Outline each Plasmodium falciparum-infected red blood cell.
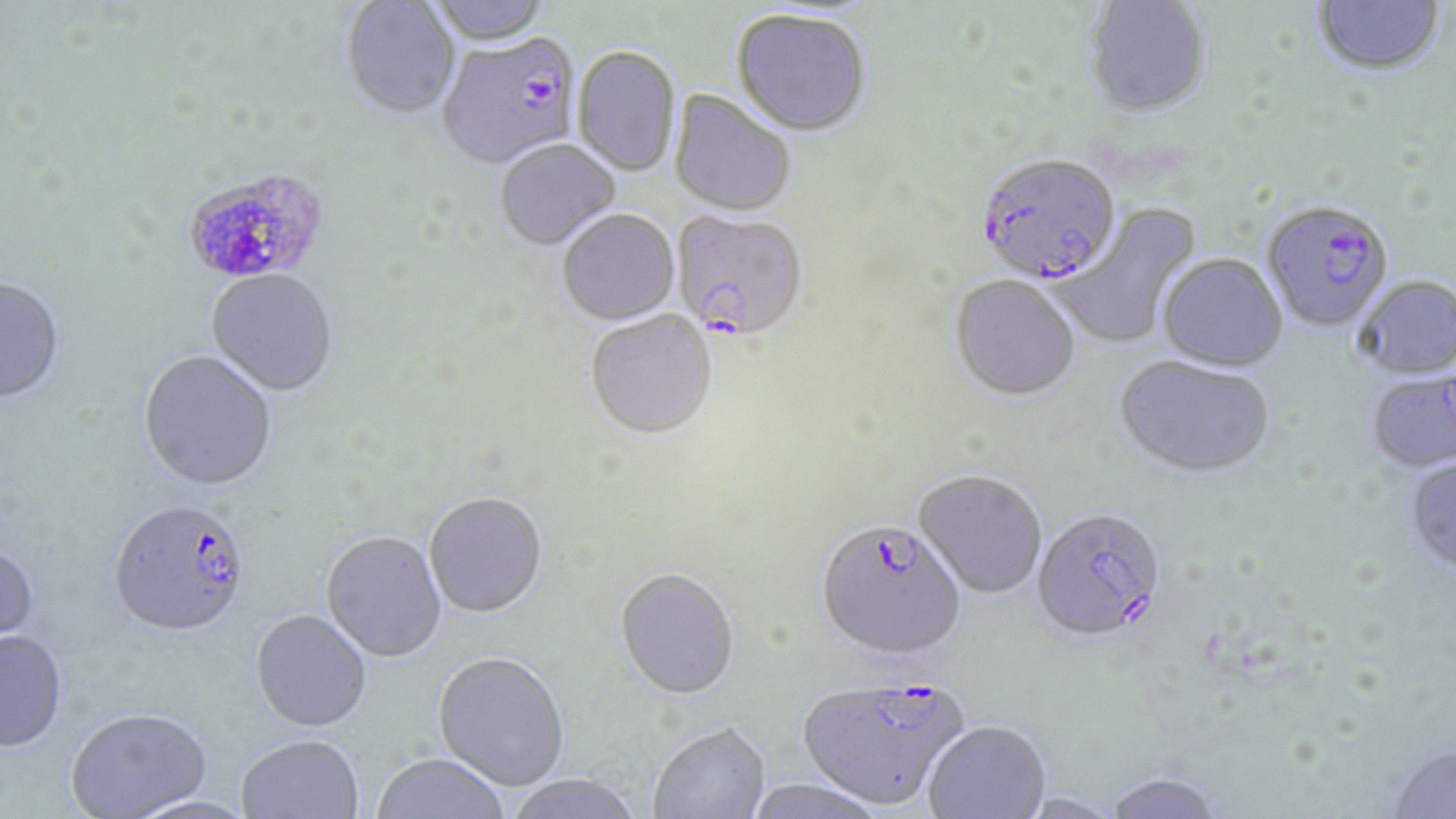

Approximate bounding boxes as named x1/y1/x2/y2 corners in pixels.
Plasmodium falciparum-infected red blood cells (subset): (x1=437, y1=35, x2=583, y2=173), (x1=976, y1=156, x2=1122, y2=289), (x1=185, y1=163, x2=332, y2=283), (x1=671, y1=211, x2=809, y2=343), (x1=108, y1=502, x2=251, y2=642), (x1=1032, y1=509, x2=1166, y2=648), (x1=815, y1=523, x2=967, y2=665), (x1=796, y1=677, x2=969, y2=813).

Summary:
  - Uninfected red blood cell locations (subset): (x1=426, y1=0, x2=554, y2=47), (x1=1312, y1=0, x2=1445, y2=78), (x1=341, y1=1, x2=460, y2=122), (x1=1083, y1=1, x2=1212, y2=122), (x1=731, y1=12, x2=872, y2=139), (x1=572, y1=48, x2=681, y2=178), (x1=668, y1=90, x2=796, y2=219), (x1=495, y1=140, x2=621, y2=253), (x1=1050, y1=202, x2=1204, y2=349), (x1=557, y1=210, x2=680, y2=328), (x1=1157, y1=255, x2=1289, y2=374), (x1=205, y1=271, x2=338, y2=398), (x1=948, y1=277, x2=1081, y2=404), (x1=1353, y1=277, x2=1456, y2=381), (x1=0, y1=278, x2=65, y2=406), (x1=585, y1=312, x2=718, y2=443), (x1=138, y1=352, x2=277, y2=495), (x1=1114, y1=357, x2=1275, y2=482), (x1=1365, y1=373, x2=1455, y2=476), (x1=1403, y1=457, x2=1456, y2=579), (x1=913, y1=471, x2=1047, y2=601), (x1=424, y1=494, x2=548, y2=620), (x1=321, y1=533, x2=446, y2=664), (x1=0, y1=545, x2=40, y2=655), (x1=614, y1=570, x2=740, y2=704), (x1=250, y1=612, x2=371, y2=735), (x1=0, y1=633, x2=67, y2=755), (x1=433, y1=654, x2=569, y2=792), (x1=66, y1=711, x2=211, y2=818), (x1=924, y1=723, x2=1051, y2=819), (x1=648, y1=724, x2=771, y2=819), (x1=236, y1=737, x2=363, y2=819), (x1=1387, y1=745, x2=1456, y2=819), (x1=371, y1=755, x2=509, y2=818), (x1=1103, y1=774, x2=1227, y2=819), (x1=504, y1=775, x2=645, y2=819), (x1=743, y1=780, x2=886, y2=819), (x1=1018, y1=795, x2=1125, y2=819), (x1=126, y1=797, x2=258, y2=819)
  - Slide-level diagnosis: Plasmodium falciparum
  - Field of view: one of a larger specimen
  - Stain: May-Grünwald-Giemsa
  - Preparation: thin blood film
  - Modality: light microscopy
  - Magnification: 1000x
  - Image size: 1456×819 pixels